Identify the parasite.
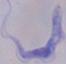

A trypanosome.

Photomicrograph. 1000x magnification.